Point out each Plasmodium parasite.
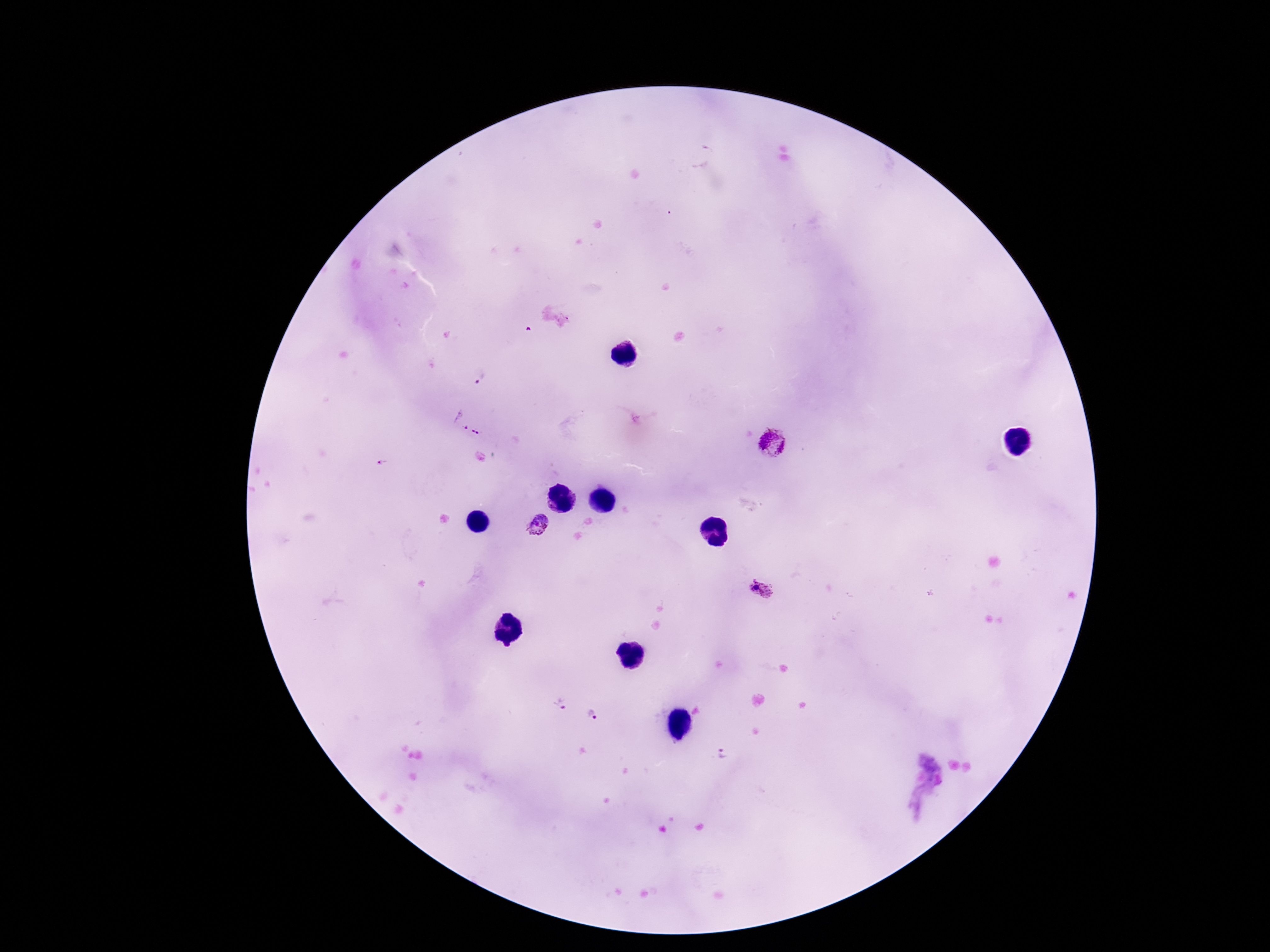
Approximate centers as (x, y) in pixels.
Plasmodium parasites: (480, 378), (460, 420), (477, 432), (775, 448), (385, 463), (538, 526), (760, 593), (559, 705), (596, 718), (724, 755).

Patient malaria status: positive. One field from this slide. 100x magnification. Giemsa-stained preparation. Thick peripheral-blood smear. Image is 1270×952 pixels. Smartphone photograph taken through the microscope eyepiece.